Describe the morphology of the red blood cells.
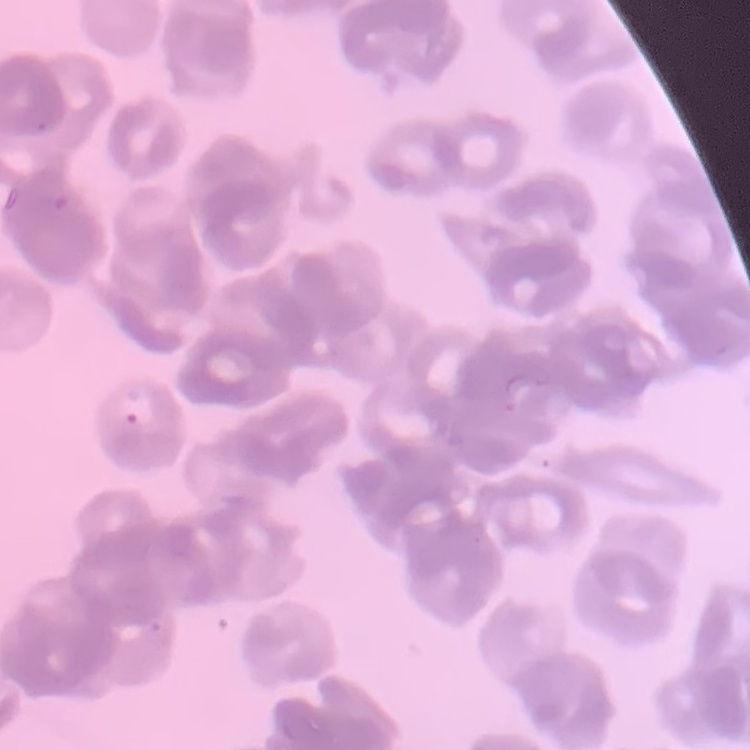

They show rouleaux formation.

Summary:
  - Preparation: thin blood smear
  - Image type: one tile cut from a larger photomicrograph
  - Stain: Field's or Giemsa